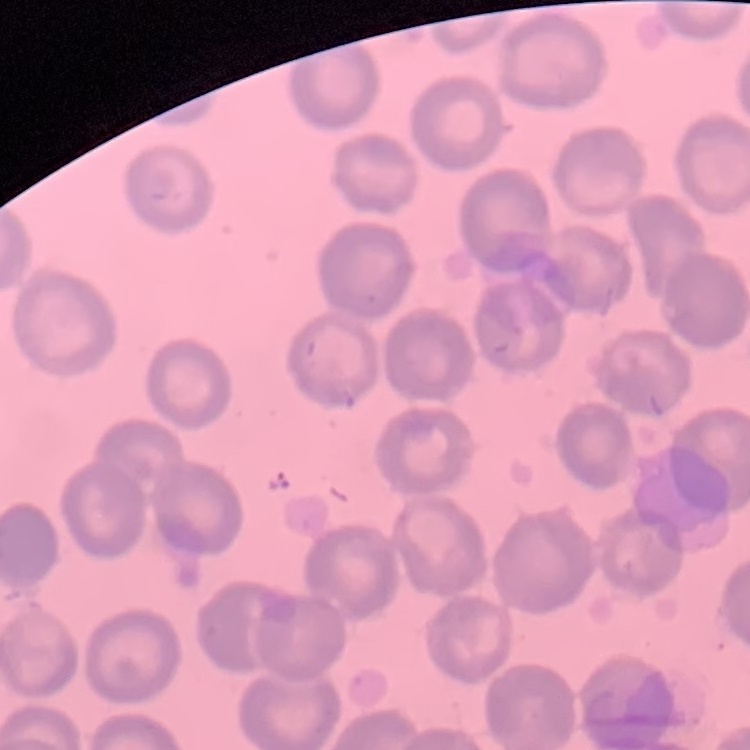

The red blood cells exhibit no rouleaux formation. One tile cut from a larger photomicrograph. Thin blood smear. Field's or Giemsa stain.